Report the malaria status of this cell.
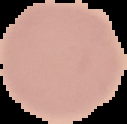

Uninfected.

Summary:
  - Preparation: thin blood film
  - Image type: segmented cell region with the area outside set to black
  - Image size: 127×124 pixels